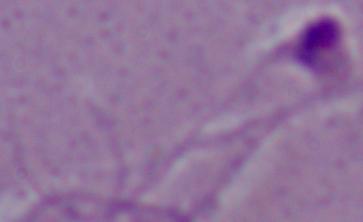
Summary:
  - Modality: micrograph
  - Identification: Leishmania
  - Magnification: 1000x